Report the malaria status.
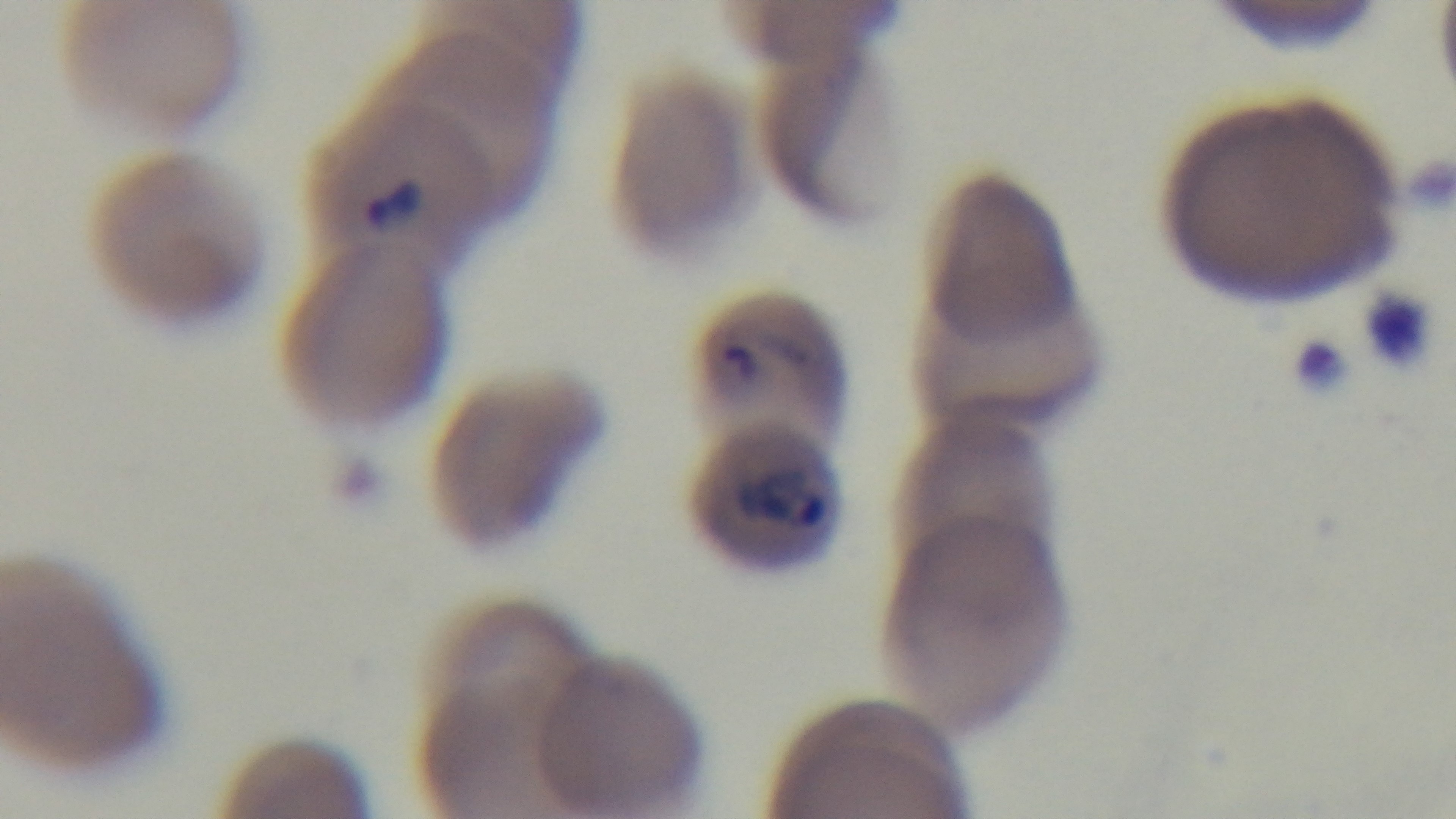

Positive.

Photomicrograph. One field from the slide. 100x oil-immersion objective. Giemsa stain. Mounted 4K digital camera. Preparation: thin blood film.